Classify this cell by malaria status.
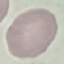
Uninfected.

Summary:
  - Stain: Giemsa
  - Capture: smartphone through the microscope eyepiece
  - Image type: automatically extracted cell patch, resized to 64 × 64 pixels
  - Preparation: thin smear